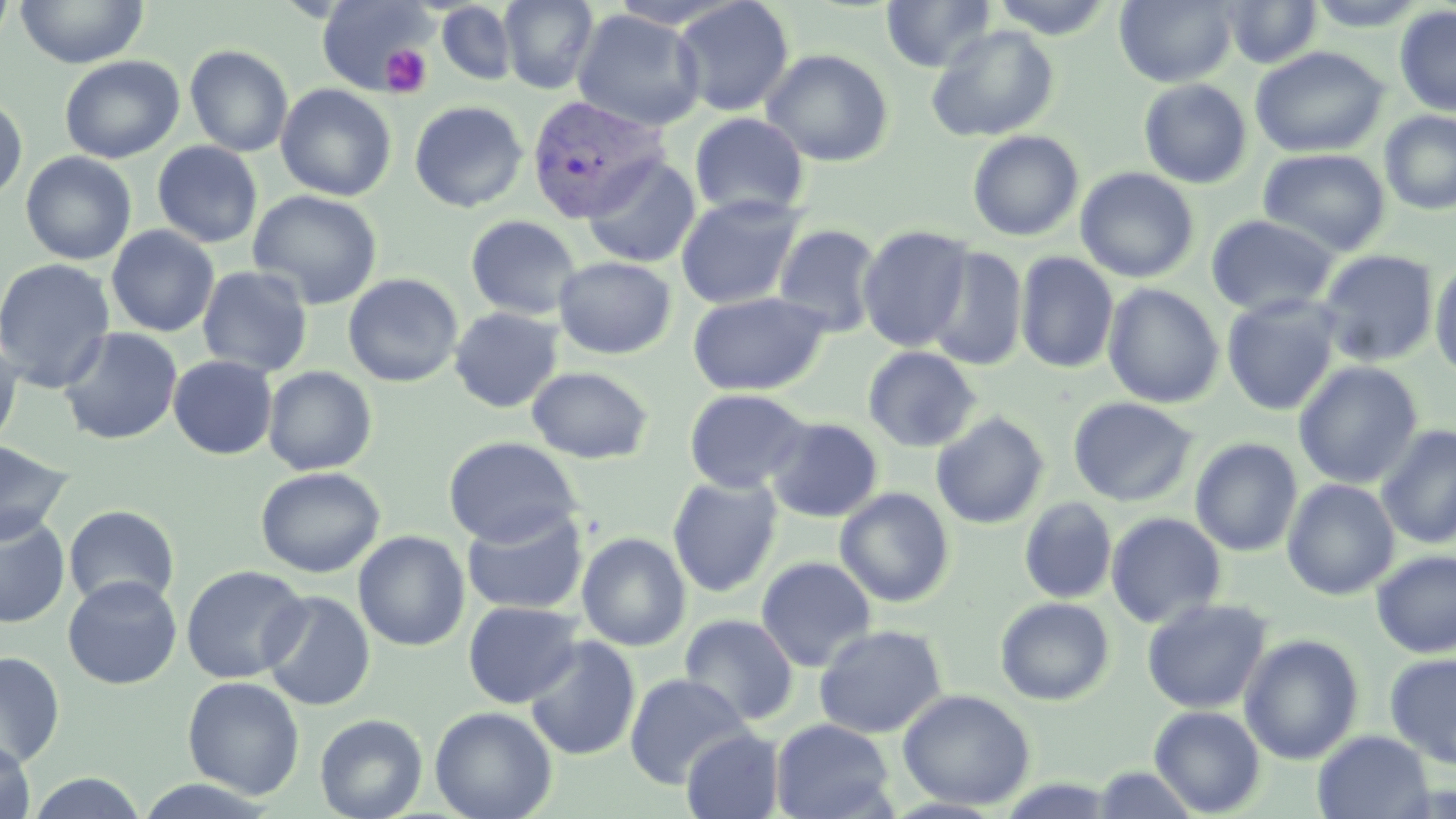

slide_level_diagnosis: Plasmodium vivax
platelet_locations: 'approximate bounding boxes as [x1, y1, x2, y2] in pixels: [380, 45, 432, 97]'
uninfected_red_blood_cell_locations: 'approximate bounding boxes as [x1, y1, x2, y2] in pixels: [0, 0, 16, 55], [15, 0, 148, 69], [671, 0, 796, 117], [881, 0, 997, 72], [987, 0, 1119, 39], [1114, 0, 1238, 88], [1221, 0, 1323, 68], [1305, 0, 1432, 31], [315, 1, 435, 95], [498, 1, 600, 94], [436, 2, 518, 86], [1394, 6, 1456, 117], [571, 9, 705, 132], [925, 24, 1060, 143], [184, 44, 293, 158], [1250, 46, 1389, 158], [761, 48, 894, 167], [59, 55, 185, 164], [1138, 79, 1253, 188], [275, 84, 397, 202], [0, 96, 28, 202], [409, 100, 528, 213], [1379, 110, 1456, 216], [689, 111, 809, 219], [966, 130, 1084, 242], [151, 141, 263, 248], [1257, 148, 1391, 257], [20, 151, 137, 265], [581, 155, 701, 269], [1075, 167, 1199, 283], [247, 189, 383, 309], [675, 193, 806, 309], [1205, 213, 1340, 318], [465, 215, 583, 321], [772, 223, 884, 337], [105, 225, 220, 337], [857, 225, 975, 352], [924, 246, 1028, 371], [1317, 250, 1439, 367], [1015, 252, 1119, 374], [553, 256, 676, 359], [0, 257, 117, 392], [1429, 259, 1456, 380], [197, 265, 314, 378], [342, 273, 464, 388], [1102, 283, 1225, 409], [687, 291, 831, 397], [1221, 294, 1342, 416], [449, 306, 564, 413], [57, 327, 183, 446], [0, 337, 24, 453], [862, 346, 981, 453], [168, 355, 278, 460], [1293, 361, 1423, 489], [262, 366, 378, 476], [526, 366, 654, 464], [684, 388, 811, 494], [1068, 396, 1198, 507], [930, 411, 1050, 529], [764, 417, 883, 523], [1375, 424, 1456, 549], [442, 436, 582, 548], [1190, 437, 1303, 557], [0, 440, 74, 545], [255, 466, 386, 579], [667, 476, 783, 598], [1282, 478, 1400, 600], [834, 488, 955, 608], [1019, 497, 1117, 604], [63, 505, 180, 611], [460, 506, 589, 616], [1105, 512, 1227, 628], [0, 513, 71, 628], [353, 531, 470, 652], [576, 532, 691, 652], [1371, 549, 1456, 659], [755, 556, 877, 672], [180, 565, 309, 684], [62, 576, 183, 690], [260, 590, 376, 712], [994, 597, 1115, 706], [1141, 597, 1272, 714], [463, 601, 584, 708], [679, 614, 800, 726], [813, 624, 948, 739], [1239, 633, 1364, 765], [523, 635, 641, 761], [0, 651, 65, 770], [1384, 652, 1456, 770], [624, 673, 752, 789], [181, 676, 305, 799], [897, 688, 1035, 810], [1149, 705, 1266, 817], [429, 706, 558, 819], [314, 713, 428, 819], [770, 718, 896, 819], [681, 728, 785, 819], [1312, 730, 1434, 818], [0, 738, 36, 818], [1089, 766, 1201, 818], [25, 771, 148, 818], [129, 779, 280, 817]'
stain: May-Grünwald-Giemsa
image_size: 1456×819 pixels
magnification: 1000x
field_of_view: single
plasmodium_vivax_infected_red_blood_cell_locations: 'approximate bounding boxes as [x1, y1, x2, y2] in pixels: [526, 94, 670, 225]'
modality: light microscopy
preparation: thin blood smear